Assess this cell for malaria.
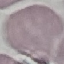

It is uninfected.

Summary:
  - Stain: Giemsa
  - Capture: smartphone through the microscope eyepiece
  - Image type: automatically extracted cell patch, resized to 64 × 64 pixels
  - Preparation: thin blood smear